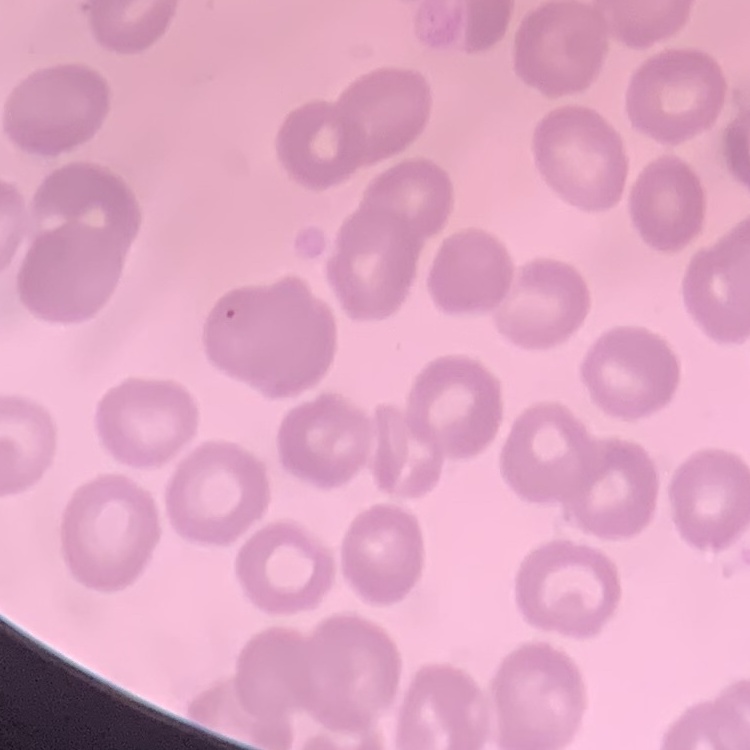
Summary:
  - Erythrocyte morphology: no rouleaux formation
  - Preparation: thin blood smear
  - Stain: Field's or Giemsa
  - Image type: one tile cut from a larger photomicrograph